Outline each blood parasite and name the species.
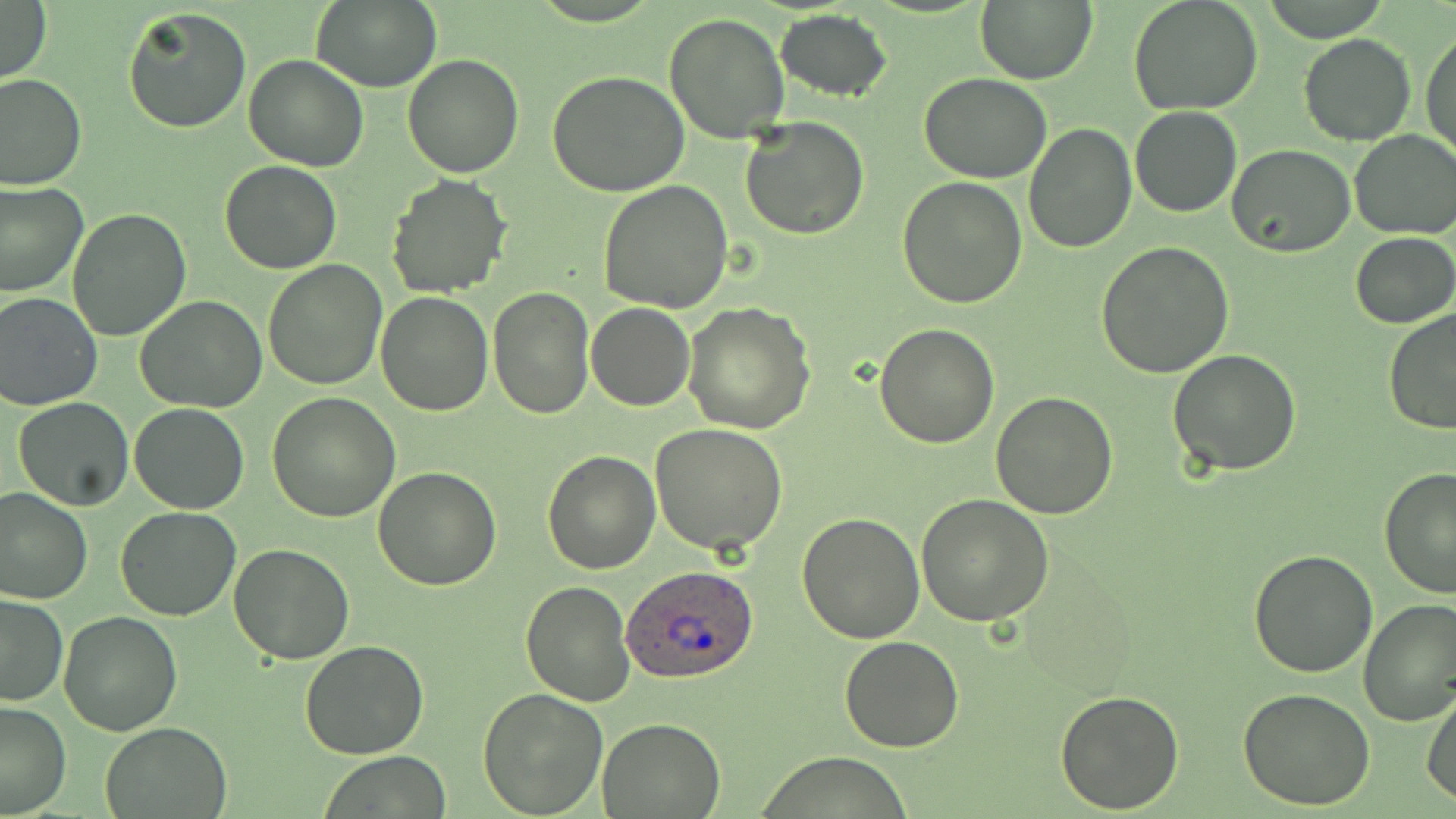
Approximate bounding boxes as (x1, y1, x2, y2) in pixels.
Plasmodium ovale-infected red blood cells: (621, 562, 762, 684).
No Plasmodium falciparum, Plasmodium malariae, Plasmodium vivax, Babesia divergens, or Trypanosoma brucei observed.

Summary:
  - Uninfected red blood cell locations: (311, 0, 441, 92), (1129, 0, 1265, 116), (0, 1, 51, 85), (975, 1, 1098, 84), (122, 6, 252, 134), (775, 9, 893, 101), (663, 13, 789, 143), (1421, 26, 1455, 163), (1297, 33, 1416, 147), (403, 53, 525, 177), (242, 55, 369, 172), (547, 71, 692, 196), (0, 73, 86, 190), (920, 73, 1053, 183), (1130, 106, 1243, 217), (739, 115, 870, 240), (1023, 122, 1137, 253), (1349, 129, 1456, 239), (1227, 145, 1355, 258), (220, 160, 342, 274), (386, 174, 513, 297), (897, 175, 1028, 307), (599, 179, 734, 313), (0, 180, 88, 298), (67, 208, 194, 340), (1351, 232, 1455, 329), (1095, 241, 1235, 378), (262, 260, 386, 391), (488, 285, 593, 417), (0, 291, 101, 411), (375, 292, 494, 416), (135, 294, 267, 414), (586, 302, 695, 411), (683, 302, 816, 432), (1381, 308, 1456, 436), (875, 322, 999, 448), (1167, 349, 1302, 478), (989, 391, 1118, 520), (268, 393, 398, 521), (13, 398, 135, 511), (129, 403, 250, 514), (649, 423, 787, 555), (541, 449, 661, 573), (1378, 466, 1455, 598), (372, 467, 502, 590), (0, 487, 92, 605), (916, 493, 1055, 627), (115, 506, 239, 621), (796, 514, 925, 643), (228, 544, 354, 663), (1248, 549, 1379, 678), (520, 578, 636, 705), (0, 594, 69, 706), (1357, 598, 1456, 726), (59, 611, 182, 735), (839, 635, 965, 753), (299, 639, 429, 760), (476, 686, 606, 816), (1055, 687, 1185, 812), (1238, 689, 1376, 810), (1422, 690, 1456, 805), (0, 701, 72, 816), (597, 717, 725, 816), (101, 720, 232, 818), (323, 752, 451, 818)
  - Slide-level diagnosis: Plasmodium ovale
  - Preparation: thin blood smear
  - Modality: optical microscopy
  - Image size: 1456×819 pixels
  - Stain: May-Grünwald-Giemsa
  - Magnification: 1000x
  - Field of view: single